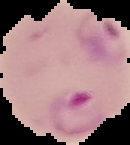

Summary:
  - Preparation: thin blood film
  - Image type: cell region segmented out of the field of view; surrounding area masked to black
  - Image size: 130×145 pixels
  - Result: Plasmodium parasites identified